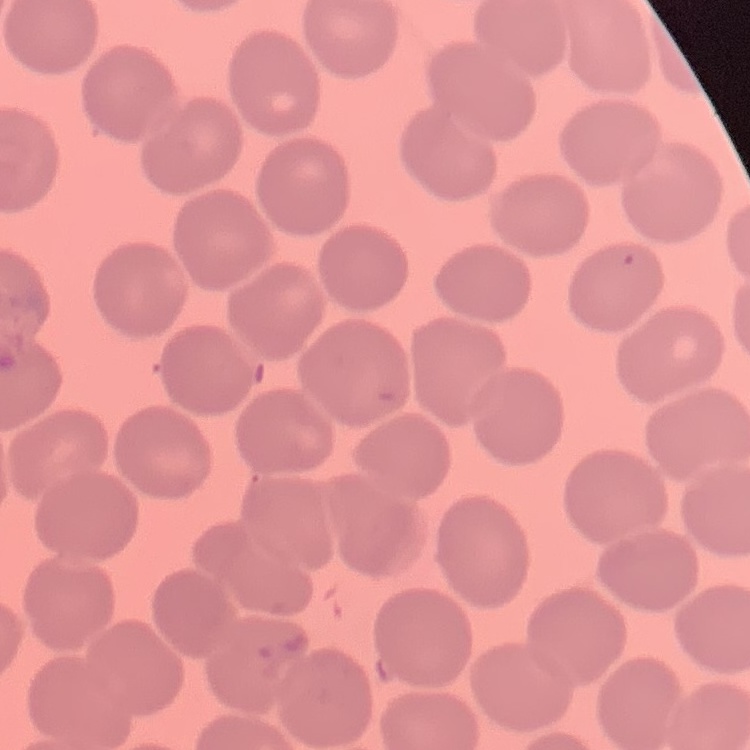 The erythrocytes show no rouleaux formation. Square crop of a larger photomicrograph. Stained with either Field's or Giemsa. Thin peripheral smear.